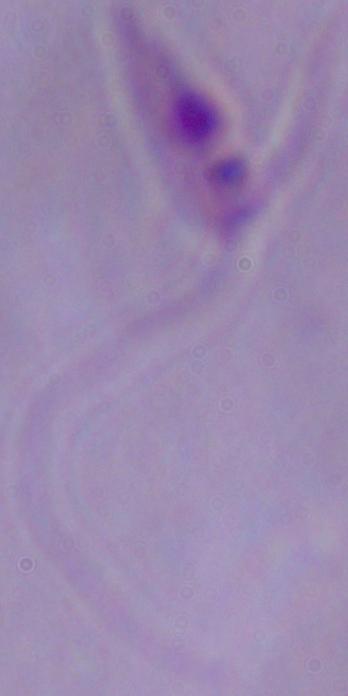

Summary:
  - Modality: micrograph
  - Identification: Leishmania
  - Magnification: 1000x